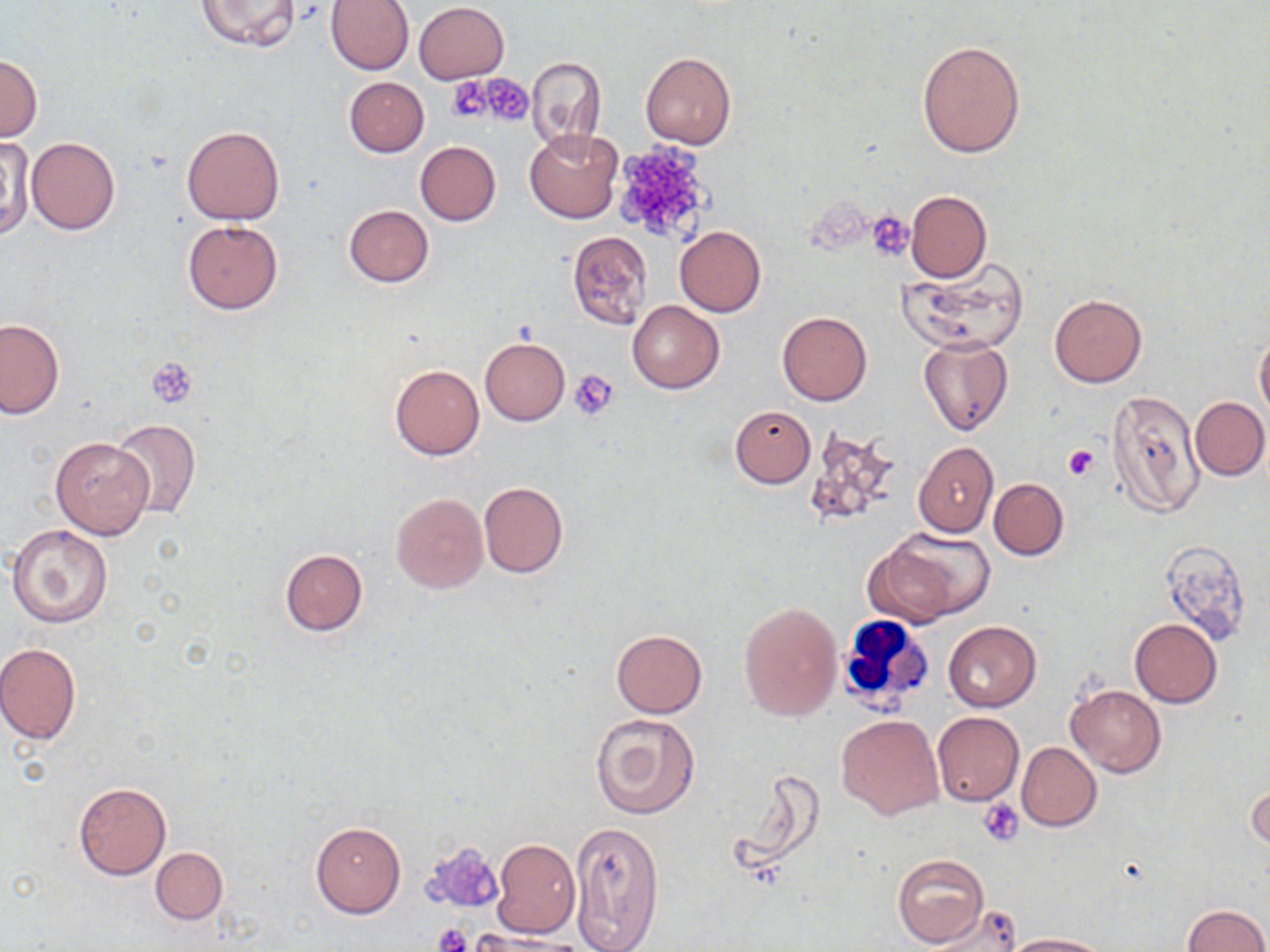

Summary:
  - Coordinate format: approximate bounding boxes as (x1, y1, x2, y2) in pixels
  - Uninfected red blood cell locations: (326, 0, 414, 74), (197, 1, 301, 51), (414, 2, 510, 84), (917, 40, 1026, 159), (640, 51, 736, 150), (0, 54, 42, 143), (526, 56, 607, 148), (344, 76, 429, 156), (181, 124, 284, 224), (525, 129, 623, 224), (1, 136, 32, 244), (26, 137, 119, 234), (415, 141, 500, 226), (906, 190, 991, 282), (343, 205, 433, 287), (182, 221, 283, 313), (674, 225, 765, 317), (566, 231, 653, 331), (900, 258, 1030, 355), (1049, 294, 1147, 388), (627, 301, 724, 393), (777, 311, 871, 406), (0, 318, 64, 419), (1254, 330, 1270, 421), (918, 336, 1011, 437), (480, 338, 569, 425), (390, 364, 485, 460), (1106, 389, 1204, 519), (1190, 396, 1269, 481), (730, 406, 816, 488), (110, 419, 200, 520), (801, 428, 906, 530), (48, 436, 154, 539), (913, 441, 998, 536), (988, 478, 1068, 560), (479, 482, 568, 578), (391, 492, 488, 595), (7, 524, 111, 628), (884, 528, 995, 620), (1159, 541, 1254, 644), (280, 548, 367, 636), (737, 599, 842, 721), (1130, 619, 1223, 707), (943, 621, 1042, 711), (610, 629, 707, 717), (0, 643, 81, 744), (1066, 683, 1166, 778), (932, 711, 1024, 806), (591, 713, 700, 820), (838, 714, 944, 820), (1017, 742, 1101, 831), (723, 770, 829, 881), (74, 781, 172, 880), (1247, 781, 1268, 852), (570, 821, 664, 952), (310, 822, 406, 919), (492, 839, 581, 938), (151, 848, 226, 924), (892, 853, 990, 948), (923, 904, 1024, 951), (1182, 904, 1269, 952), (1004, 932, 1111, 951)
  - Platelet locations: (477, 74, 533, 126), (449, 76, 497, 123), (610, 142, 713, 245), (868, 212, 914, 259), (146, 357, 198, 408), (571, 369, 621, 419), (1063, 443, 1100, 482), (981, 797, 1026, 846), (424, 846, 502, 915), (434, 924, 471, 952)
  - White blood cell locations: (834, 612, 933, 714)
  - Slide-level diagnosis: negative for blood parasites
  - Modality: light microscopy
  - Stain: May-Grünwald-Giemsa
  - Preparation: thin blood film
  - Magnification: 1000x
  - Image size: 1270×952 pixels
  - Field of view: one of a larger specimen